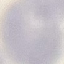
result = no malaria parasites detected
preparation = thin smear
image type = cell patch, automatically extracted from a larger field of view and resized to 64 × 64 pixels
stain = Giemsa
capture = smartphone through the microscope eyepiece